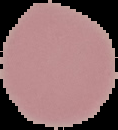

image type = segmented cell region on a black background
preparation = thin blood smear
image size = 118×130 pixels
result = negative for Plasmodium parasites